Identify the parasite.
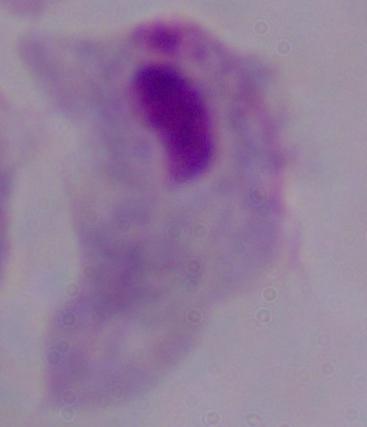
A trichomonad.

Captured at 1000x magnification. Micrograph.